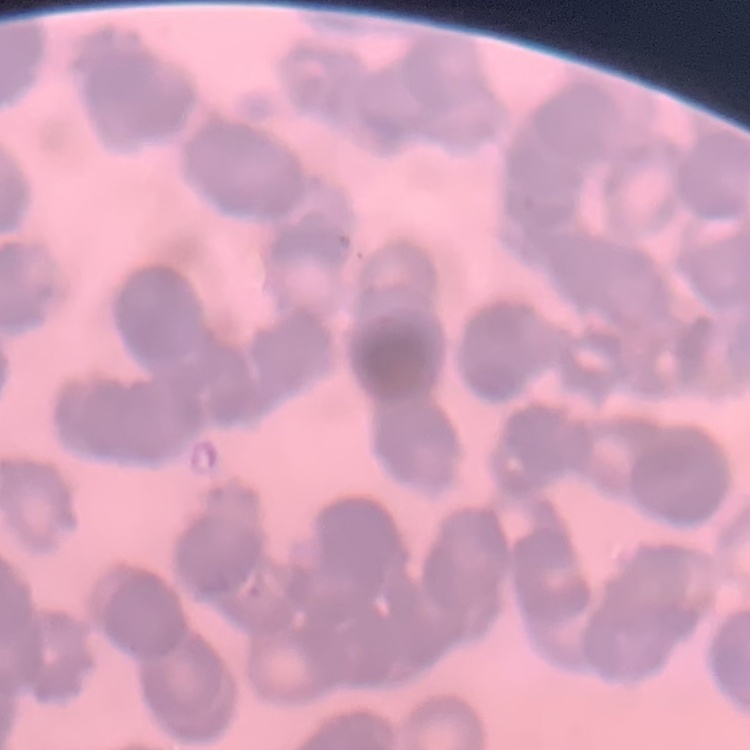 The erythrocytes show rouleaux formation. Field's or Giemsa stain. One tile cut from a larger photomicrograph. Thin blood film.